Assess this cell for malaria.
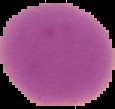

Uninfected.

preparation = thin blood film
image type = segmented cell region with the area outside set to black
image size = 115×109 pixels